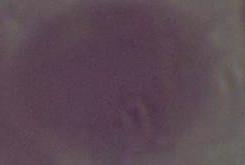
1000x magnification. Photomicrograph. An erythrocyte is seen.